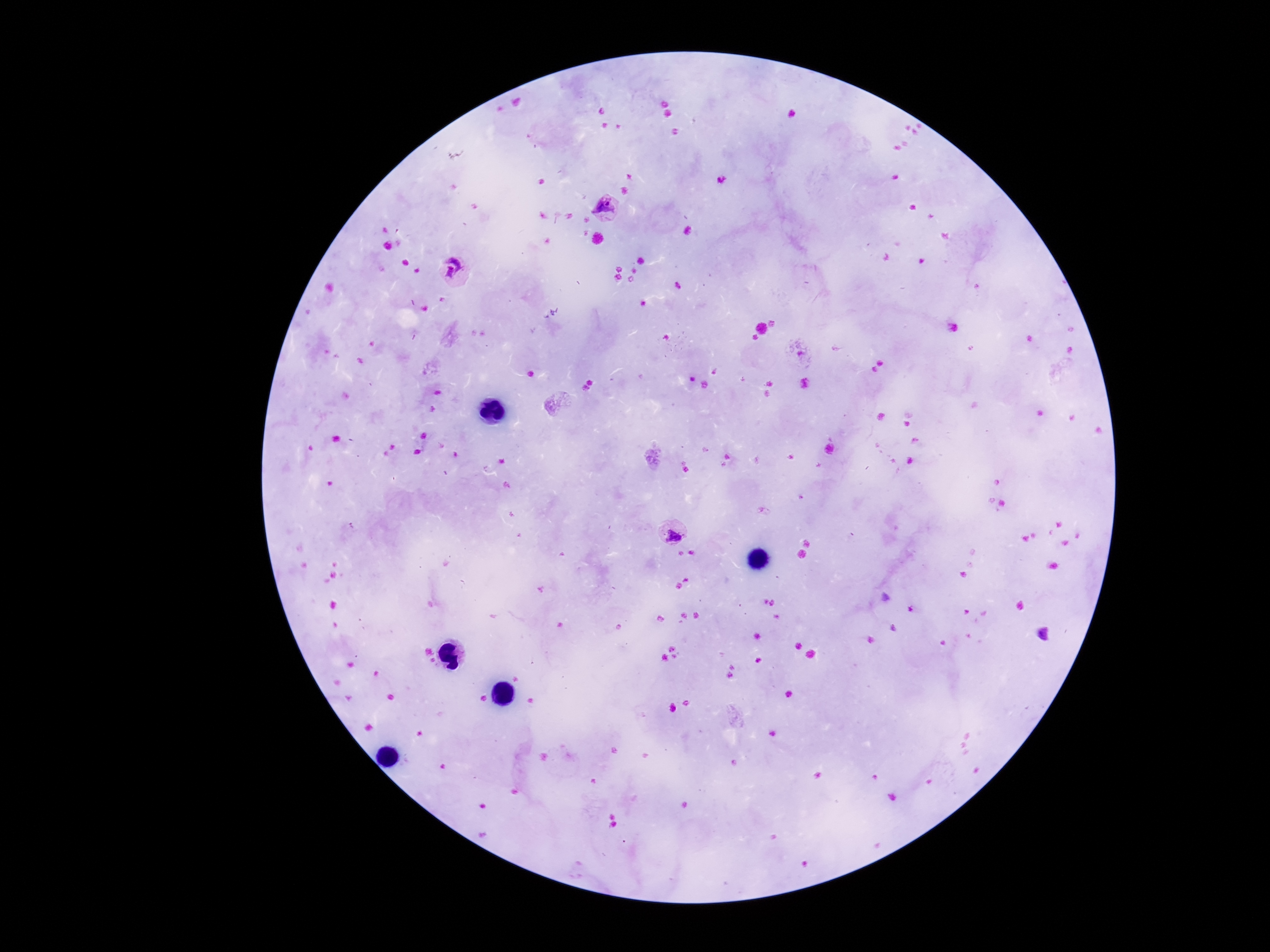
Approximate object centers, in pixels from the top-left corner. Plasmodium parasite locations: (x=609, y=208), (x=454, y=272), (x=673, y=530). Thick blood smear. Photographed through the microscope eyepiece with a smartphone camera. Image is 1270×952 pixels. 100x magnification. Single field of view. Giemsa stain. Patient malaria status: positive.